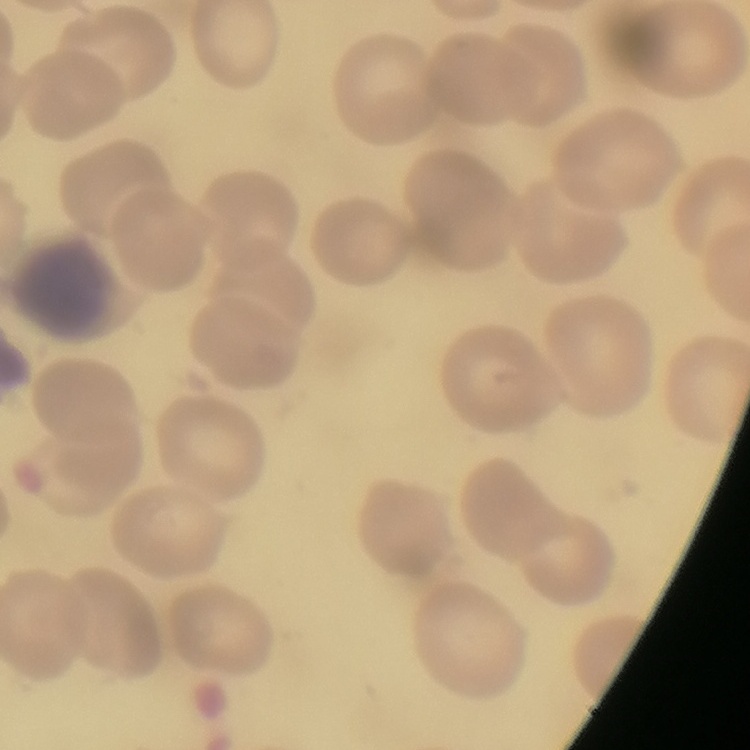
The red blood cells show no rouleaux formation. Field's or Giemsa stain. One tile cut from a larger photomicrograph. Thin peripheral smear.